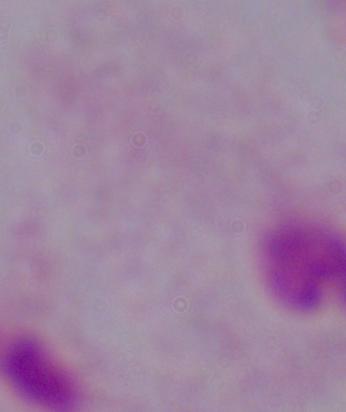

Captured at 1000x magnification. Photomicrograph. A trichomonad is seen.